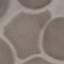
malaria status = uninfected
stain = Giemsa
capture = smartphone through the microscope eyepiece
image type = automatically extracted cell patch, resized to 64 × 64 pixels
preparation = thin blood film